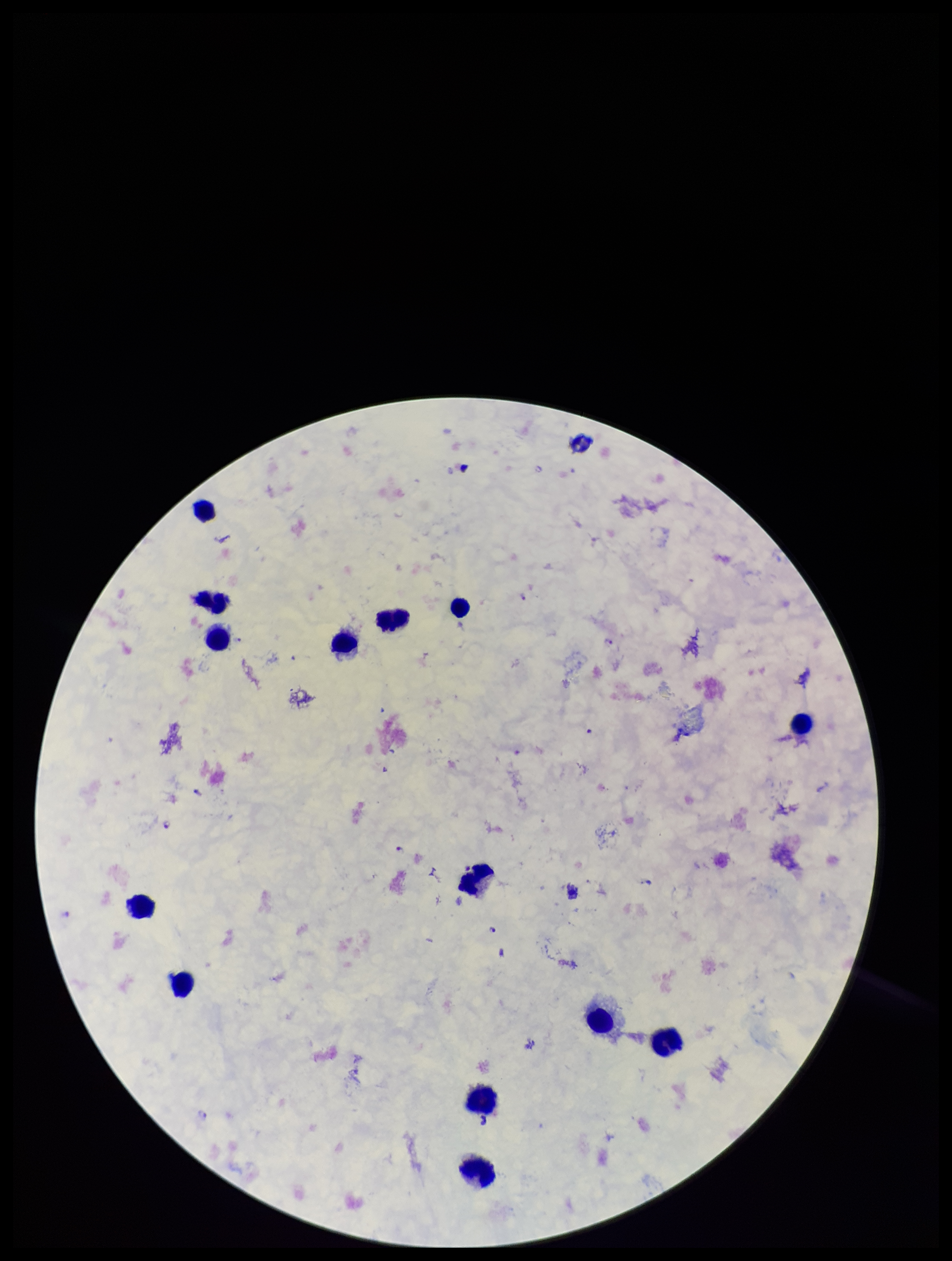 Plasmodium parasites: seen. Single field of view. Parasite count: 10. Image is 952×1261 pixels. Smartphone photograph taken through the eyepiece of a microscope. Species reported for this patient: Plasmodium falciparum. Leukocyte count: 14. Patient malaria status: positive. Preparation: thick. Giemsa stain.